Locate every malaria parasite and every leukocyte.
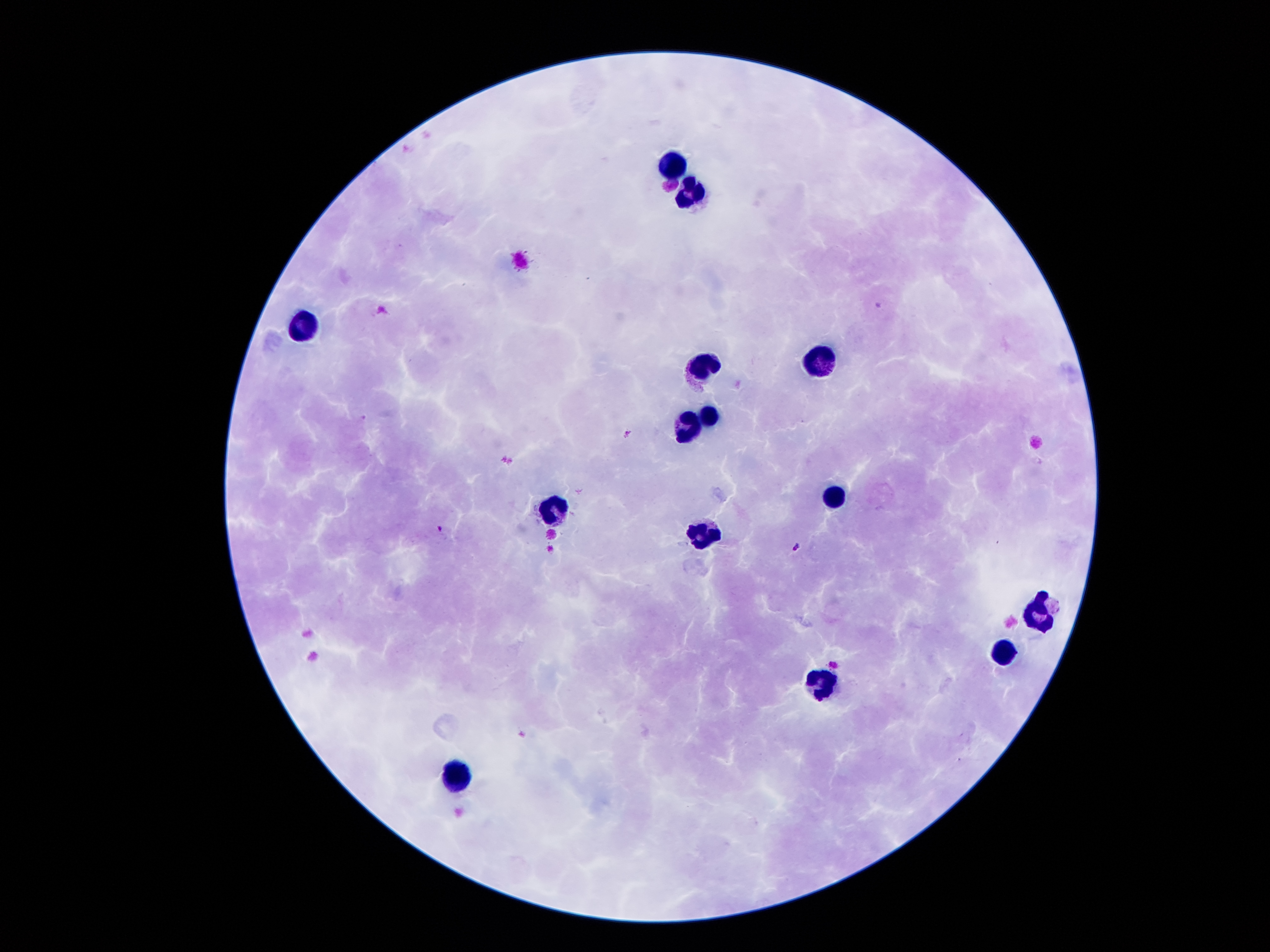
Approximate object centers, in pixels from the top-left corner.
Malaria parasites: (x=878, y=302), (x=626, y=432), (x=438, y=528), (x=796, y=546), (x=832, y=663).
Leukocytes: (x=675, y=165), (x=691, y=195), (x=304, y=326), (x=823, y=361), (x=703, y=367), (x=709, y=415), (x=687, y=426), (x=832, y=498), (x=552, y=509), (x=700, y=533), (x=1036, y=606), (x=1002, y=656), (x=822, y=683), (x=453, y=779).

magnification = 100x
field of view = one from this slide
capture = smartphone through the microscope eyepiece
image size = 1270×952 pixels
stain = Giemsa
preparation = thick blood smear
patient malaria status = positive for Plasmodium falciparum